Assess this cell for malaria.
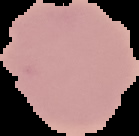

Uninfected.

image size = 139×136 pixels
preparation = thin blood smear
image type = segmented cell region with the area outside set to black